Name the parasite shown.
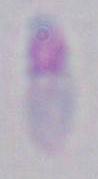

Toxoplasma gondii.

Summary:
  - Modality: photomicrograph
  - Magnification: 1000x